State the blood parasite species.
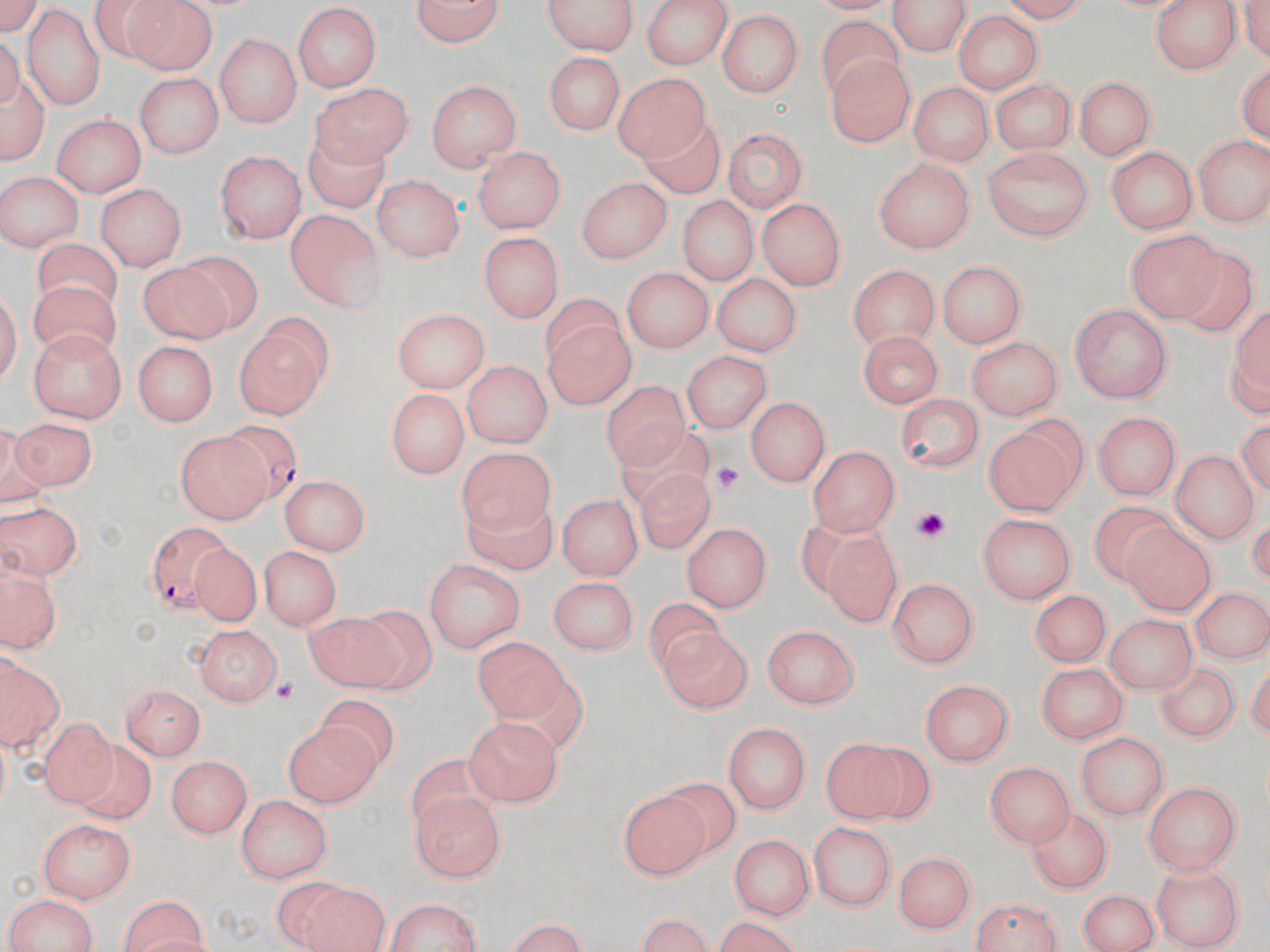
Plasmodium falciparum.

Summary:
  - Coordinate format: approximate bounding boxes as (x1,y1)-(x2,y2) corner pairs in pixels
  - Plasmodium falciparum-infected red blood cell locations: (216,422)-(303,504), (138,522)-(246,612)
  - Uninfected red blood cell locations: (411,0)-(507,50), (538,0)-(641,56), (639,0)-(732,69), (892,0)-(968,59), (121,1)-(217,74), (1150,1)-(1239,75), (22,7)-(106,107), (292,7)-(382,93), (717,9)-(807,100), (815,12)-(911,97), (950,14)-(1045,98), (0,32)-(46,167), (213,33)-(303,127), (546,53)-(624,135), (824,53)-(916,147), (1238,57)-(1269,150), (615,69)-(709,159), (135,70)-(225,159), (1073,74)-(1157,164), (424,77)-(524,173), (989,78)-(1077,153), (911,79)-(997,165), (315,82)-(414,167), (641,110)-(723,197), (52,112)-(147,199), (721,128)-(805,214), (296,132)-(401,219), (1192,133)-(1267,225), (1105,144)-(1196,234), (473,145)-(565,233), (983,147)-(1090,241), (215,149)-(305,242), (873,159)-(976,255), (0,171)-(80,254), (371,174)-(463,263), (577,174)-(674,262), (96,182)-(185,272), (675,197)-(759,286), (755,197)-(844,290), (287,208)-(386,312), (1125,228)-(1220,321), (480,233)-(561,322), (31,236)-(126,316), (1170,248)-(1261,341), (140,253)-(244,343), (938,261)-(1029,347), (846,263)-(941,348), (623,266)-(717,352), (28,273)-(122,361), (714,273)-(801,358), (1226,298)-(1268,421), (1071,305)-(1174,402), (390,309)-(491,391), (232,314)-(331,420), (543,322)-(640,413), (31,331)-(125,423), (858,332)-(943,411), (966,337)-(1066,421), (135,340)-(218,425), (681,351)-(770,433), (458,358)-(549,444), (601,378)-(695,477), (383,388)-(473,480), (895,393)-(982,471), (746,396)-(826,487), (1094,411)-(1180,503), (11,415)-(92,493), (983,416)-(1088,510), (619,418)-(711,507), (175,427)-(272,520), (456,445)-(559,540), (810,446)-(900,534), (1168,448)-(1257,541), (634,464)-(720,557), (277,478)-(367,558), (457,487)-(558,576), (561,492)-(645,579), (0,498)-(78,579), (1086,499)-(1189,587), (789,505)-(890,595), (976,512)-(1074,604), (681,518)-(775,612), (1119,518)-(1220,621), (821,532)-(903,627), (260,543)-(342,632), (185,547)-(262,622), (424,557)-(526,651), (4,565)-(57,652), (550,574)-(637,656), (888,578)-(981,670), (1193,586)-(1270,661), (1030,589)-(1116,669), (644,593)-(729,672), (305,606)-(408,692), (1103,612)-(1196,690), (194,623)-(282,704), (658,624)-(756,715), (765,624)-(860,707), (469,638)-(565,721), (1154,652)-(1249,749), (2,657)-(59,750), (1034,663)-(1129,742), (122,680)-(209,761), (921,682)-(1011,768), (317,695)-(396,774), (463,714)-(561,805), (34,715)-(118,805), (284,719)-(386,805), (722,721)-(812,814), (1078,732)-(1167,818), (824,736)-(929,828), (80,738)-(160,826), (404,751)-(503,837), (169,753)-(250,836), (989,762)-(1073,849), (662,775)-(742,854), (1146,780)-(1241,875), (618,787)-(711,876), (414,790)-(509,884), (237,795)-(334,883), (1028,803)-(1111,889), (39,817)-(136,904), (809,823)-(897,913), (727,834)-(812,921), (896,849)-(975,932), (1149,859)-(1247,945), (296,882)-(388,952), (1074,891)-(1159,952), (0,893)-(103,952), (112,895)-(213,950), (385,895)-(485,952), (967,896)-(1070,952), (629,914)-(723,950), (701,920)-(812,951), (497,921)-(597,950)
  - Platelet locations: (709,457)-(748,496), (907,503)-(950,542), (269,678)-(303,708)
  - Field of view: single
  - Image size: 1270×952 pixels
  - Preparation: thin blood film
  - Stain: May-Grünwald-Giemsa
  - Modality: optical microscopy
  - Magnification: 1000x